Locate and identify every blood parasite.
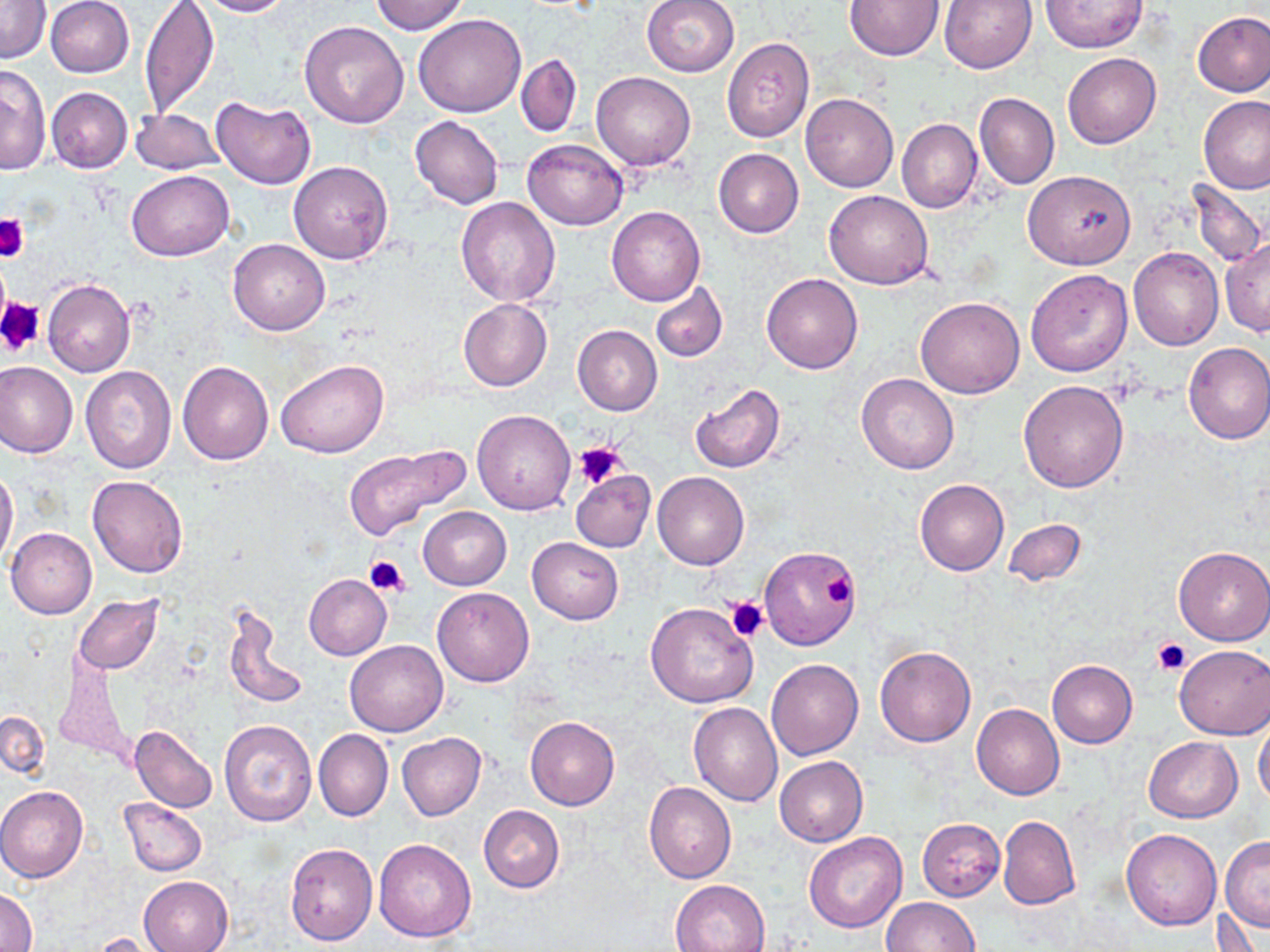
No blood parasites seen.

Summary:
  - Coordinate format: approximate bounding boxes as (x1,y1)-(x2,y2) corner pairs in pixels
  - Platelet locations: (0,213)-(28,261), (0,298)-(44,357), (573,440)-(628,489), (364,555)-(411,598), (817,570)-(857,612), (725,595)-(770,641), (1152,638)-(1190,675)
  - Uninfected red blood cell locations: (45,0)-(135,78), (139,0)-(220,117), (197,0)-(292,17), (369,0)-(468,35), (641,0)-(740,77), (940,0)-(1037,73), (1,1)-(50,64), (845,1)-(944,60), (1040,1)-(1148,52), (1192,10)-(1270,97), (414,14)-(527,118), (299,21)-(409,128), (722,38)-(814,142), (1063,51)-(1161,148), (516,53)-(582,138), (0,65)-(50,176), (591,72)-(695,171), (46,88)-(132,173), (800,92)-(899,193), (973,92)-(1060,189), (210,95)-(316,189), (1199,96)-(1270,194), (130,108)-(222,175), (409,116)-(503,209), (897,118)-(983,213), (523,138)-(627,230), (713,149)-(804,238), (289,161)-(393,264), (127,169)-(232,261), (1023,169)-(1135,269), (1187,179)-(1267,267), (824,190)-(934,289), (456,196)-(560,306), (607,206)-(705,307), (229,238)-(330,336), (1221,241)-(1270,336), (1129,247)-(1223,350), (1025,268)-(1132,377), (762,272)-(864,374), (42,277)-(135,378), (651,281)-(728,363), (915,296)-(1025,398), (458,299)-(551,391), (573,325)-(663,415), (1182,342)-(1270,444), (277,359)-(388,459), (0,360)-(78,458), (177,361)-(274,466), (81,365)-(177,473), (856,373)-(960,474), (1018,380)-(1130,492), (688,382)-(787,473), (472,409)-(576,515), (343,443)-(470,542), (0,466)-(19,572), (571,470)-(655,552), (653,471)-(749,569), (86,476)-(188,578), (915,479)-(1009,576), (418,507)-(511,590), (1003,518)-(1085,587), (6,527)-(97,618), (527,537)-(624,624), (1174,546)-(1270,645), (759,547)-(859,650), (304,573)-(391,660), (433,587)-(534,687), (73,595)-(164,674), (646,601)-(759,708), (223,607)-(310,713), (345,640)-(448,736), (874,645)-(976,747), (1175,645)-(1270,739), (54,653)-(134,768), (766,659)-(864,760), (1047,660)-(1137,748), (689,702)-(783,806), (972,704)-(1065,799), (0,709)-(49,780), (525,716)-(619,810), (1254,716)-(1270,810), (218,718)-(316,827), (128,724)-(218,812), (313,728)-(393,822), (397,732)-(485,820), (1144,737)-(1242,822), (775,756)-(868,847), (644,781)-(736,883), (0,786)-(88,883), (119,797)-(207,876), (479,805)-(564,892), (997,815)-(1079,909), (917,819)-(1006,900), (1121,829)-(1221,930), (803,833)-(906,933), (1220,836)-(1270,932), (373,838)-(477,943), (284,842)-(377,945), (138,875)-(234,952), (670,878)-(771,952), (1,887)-(35,951), (882,897)-(979,951), (89,931)-(168,952)
  - Slide-level diagnosis: negative for blood parasites
  - Image size: 1270×952 pixels
  - Preparation: thin blood film
  - Stain: May-Grünwald-Giemsa
  - Magnification: 1000x
  - Modality: optical microscopy
  - Field of view: one of a larger specimen